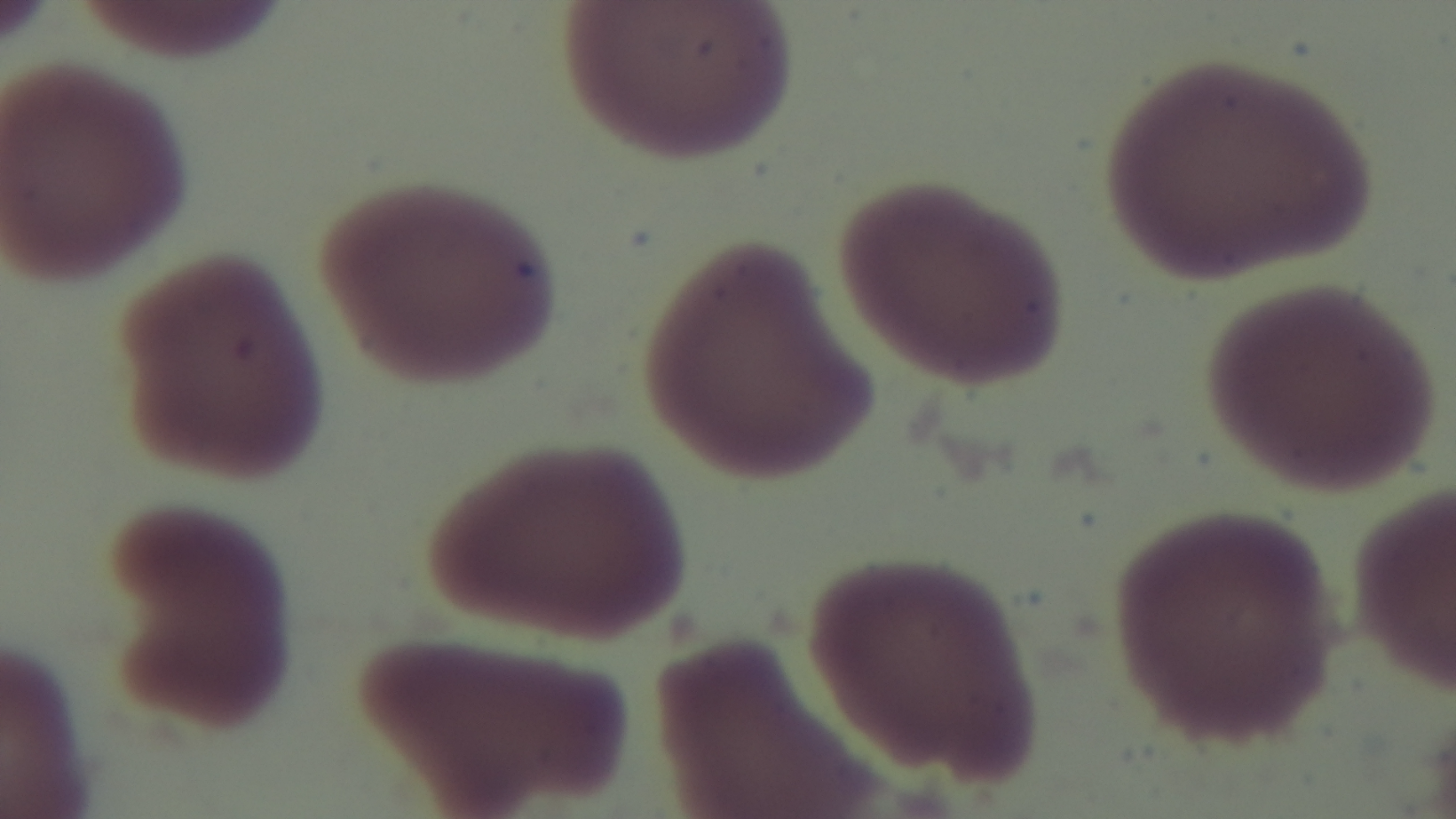

Malaria status: negative. Giemsa stain. Photomicrograph. Preparation: thin smear. 100x oil-immersion objective. One field from the slide. Mounted 4K digital camera.